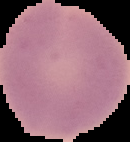

result = no malaria parasites seen
image type = cell region segmented out of the field of view; surrounding area masked to black
image size = 130×142 pixels
preparation = thin blood smear